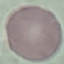

{
  "malaria_status": "uninfected",
  "preparation": "thin smear",
  "stain": "Giemsa",
  "capture": "smartphone through the microscope eyepiece",
  "image_type": "automatically extracted cell patch, resized to 64 × 64 pixels"
}